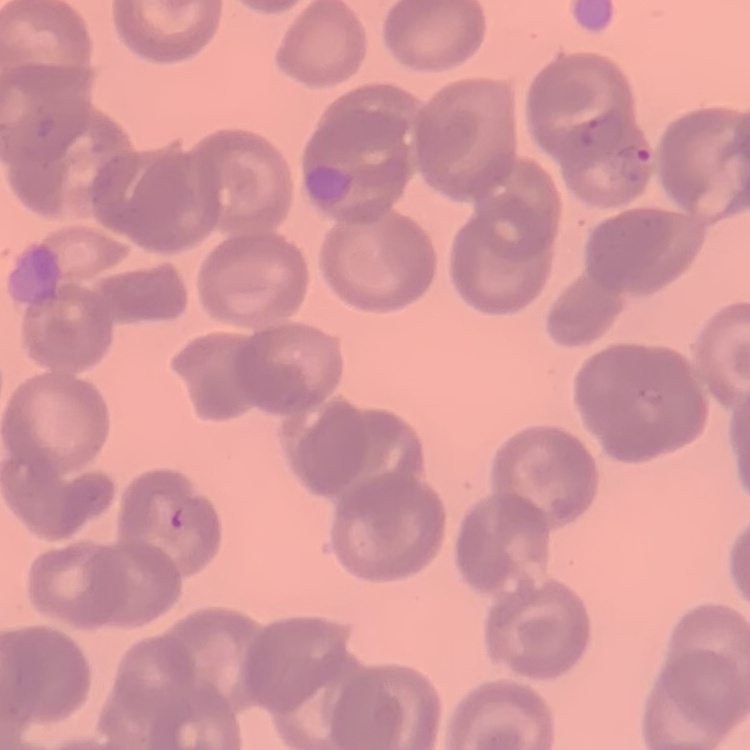

The red blood cells show no rouleaux formation. Thin blood film. One tile cut from a larger photomicrograph. Field's or Giemsa stain.